Classify this cell by malaria status.
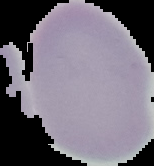

It is uninfected.

Summary:
  - Preparation: thin blood smear
  - Image size: 154×166 pixels
  - Image type: segmented cell region with the area outside set to black